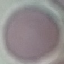

Summary:
  - Result: no malaria parasites detected
  - Stain: Giemsa
  - Capture: smartphone camera at the microscope eyepiece
  - Preparation: thin blood film
  - Image type: cell patch, automatically extracted from a larger field of view and resized to 64 × 64 pixels